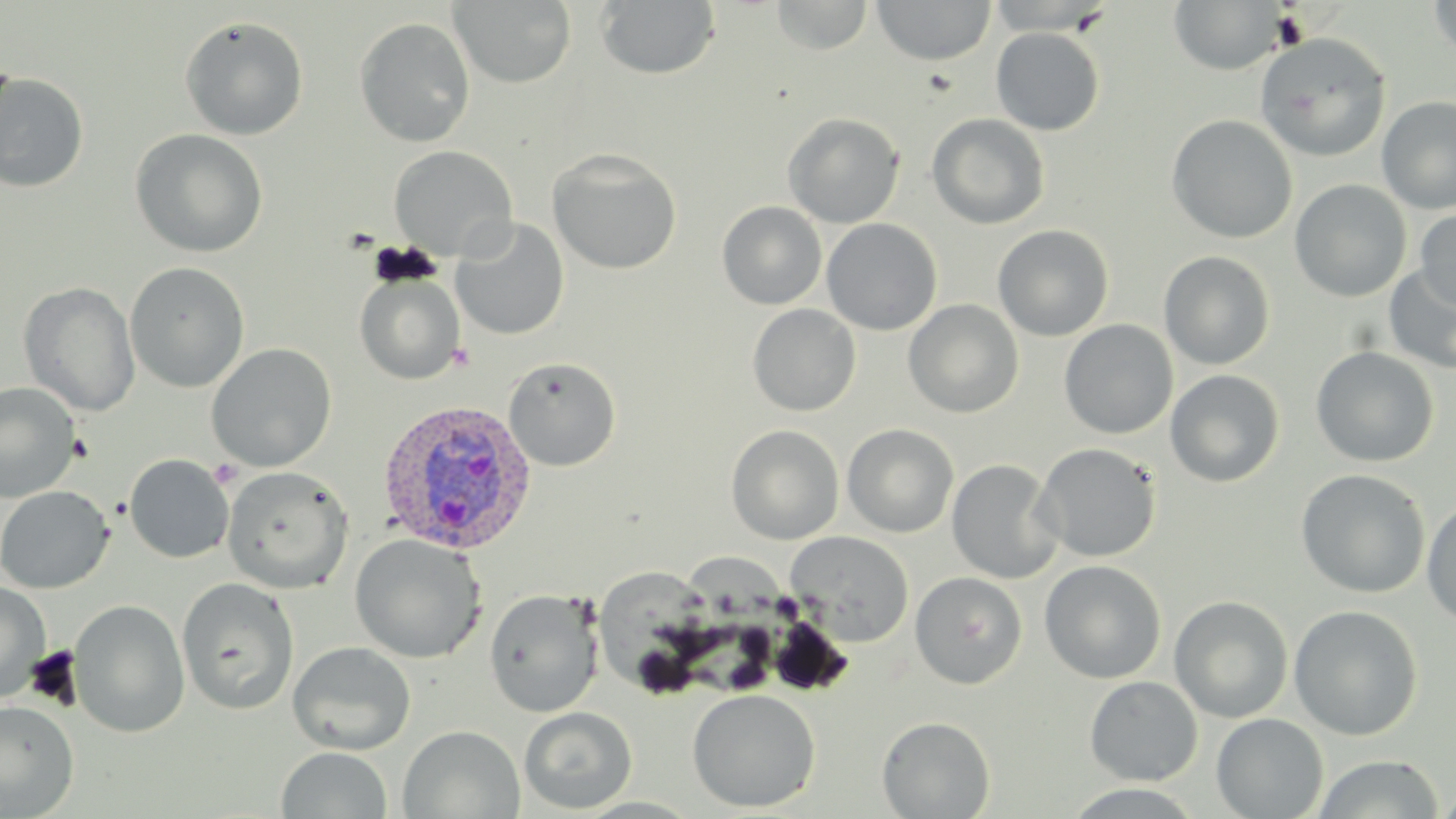

{
  "slide_level_diagnosis": "Plasmodium vivax",
  "uninfected_red_blood_cell_locations": "approximate bounding boxes as named x1/y1/x2/y2 corners in pixels: (x1=771, y1=0, x2=872, y2=55), (x1=1426, y1=0, x2=1456, y2=60), (x1=450, y1=1, x2=576, y2=88), (x1=595, y1=1, x2=722, y2=80), (x1=871, y1=1, x2=996, y2=66), (x1=1168, y1=1, x2=1288, y2=74), (x1=179, y1=15, x2=309, y2=141), (x1=354, y1=17, x2=476, y2=147), (x1=990, y1=27, x2=1105, y2=135), (x1=1255, y1=33, x2=1390, y2=162), (x1=0, y1=72, x2=90, y2=192), (x1=1376, y1=96, x2=1456, y2=214), (x1=782, y1=113, x2=905, y2=228), (x1=926, y1=113, x2=1050, y2=230), (x1=1166, y1=114, x2=1298, y2=243), (x1=129, y1=129, x2=268, y2=258), (x1=388, y1=145, x2=517, y2=261), (x1=547, y1=148, x2=683, y2=274), (x1=1289, y1=179, x2=1412, y2=302), (x1=716, y1=201, x2=827, y2=310), (x1=1415, y1=208, x2=1456, y2=312), (x1=451, y1=218, x2=569, y2=341), (x1=822, y1=218, x2=942, y2=335), (x1=993, y1=224, x2=1114, y2=341), (x1=1158, y1=250, x2=1275, y2=370), (x1=124, y1=261, x2=250, y2=393), (x1=1384, y1=264, x2=1456, y2=374), (x1=354, y1=271, x2=465, y2=385), (x1=18, y1=281, x2=140, y2=417), (x1=903, y1=299, x2=1024, y2=418), (x1=747, y1=304, x2=861, y2=416), (x1=1059, y1=319, x2=1178, y2=439), (x1=206, y1=343, x2=337, y2=471), (x1=1310, y1=346, x2=1439, y2=467), (x1=503, y1=356, x2=621, y2=471), (x1=1165, y1=369, x2=1285, y2=487), (x1=0, y1=382, x2=82, y2=504), (x1=842, y1=423, x2=959, y2=538), (x1=726, y1=424, x2=845, y2=545), (x1=1034, y1=443, x2=1162, y2=562), (x1=124, y1=454, x2=234, y2=563), (x1=946, y1=459, x2=1063, y2=584), (x1=222, y1=465, x2=354, y2=593), (x1=1295, y1=469, x2=1431, y2=598), (x1=0, y1=485, x2=114, y2=593), (x1=1422, y1=496, x2=1456, y2=627), (x1=785, y1=531, x2=915, y2=646), (x1=348, y1=533, x2=487, y2=663), (x1=692, y1=553, x2=800, y2=694), (x1=1039, y1=559, x2=1167, y2=683), (x1=599, y1=568, x2=725, y2=704), (x1=910, y1=571, x2=1027, y2=688), (x1=177, y1=578, x2=300, y2=715), (x1=0, y1=581, x2=52, y2=703), (x1=483, y1=588, x2=604, y2=718), (x1=1170, y1=595, x2=1294, y2=723), (x1=69, y1=599, x2=190, y2=738), (x1=1288, y1=605, x2=1423, y2=740), (x1=287, y1=641, x2=416, y2=756), (x1=1084, y1=676, x2=1203, y2=786), (x1=687, y1=688, x2=821, y2=812), (x1=0, y1=700, x2=80, y2=817), (x1=518, y1=706, x2=637, y2=814), (x1=1211, y1=713, x2=1329, y2=819), (x1=877, y1=716, x2=995, y2=818), (x1=398, y1=725, x2=525, y2=818), (x1=275, y1=747, x2=393, y2=819), (x1=1313, y1=755, x2=1446, y2=818), (x1=1434, y1=784, x2=1456, y2=817)",
  "stain": "May-Grünwald-Giemsa",
  "preparation": "thin blood film",
  "image_size": "1456×819 pixels",
  "magnification": "1000x",
  "field_of_view": "one of a larger specimen",
  "plasmodium_vivax_infected_red_blood_cell_locations": "approximate bounding boxes as named x1/y1/x2/y2 corners in pixels: (x1=376, y1=398, x2=536, y2=555)",
  "modality": "optical microscopy"
}